Locate and identify every blood parasite.
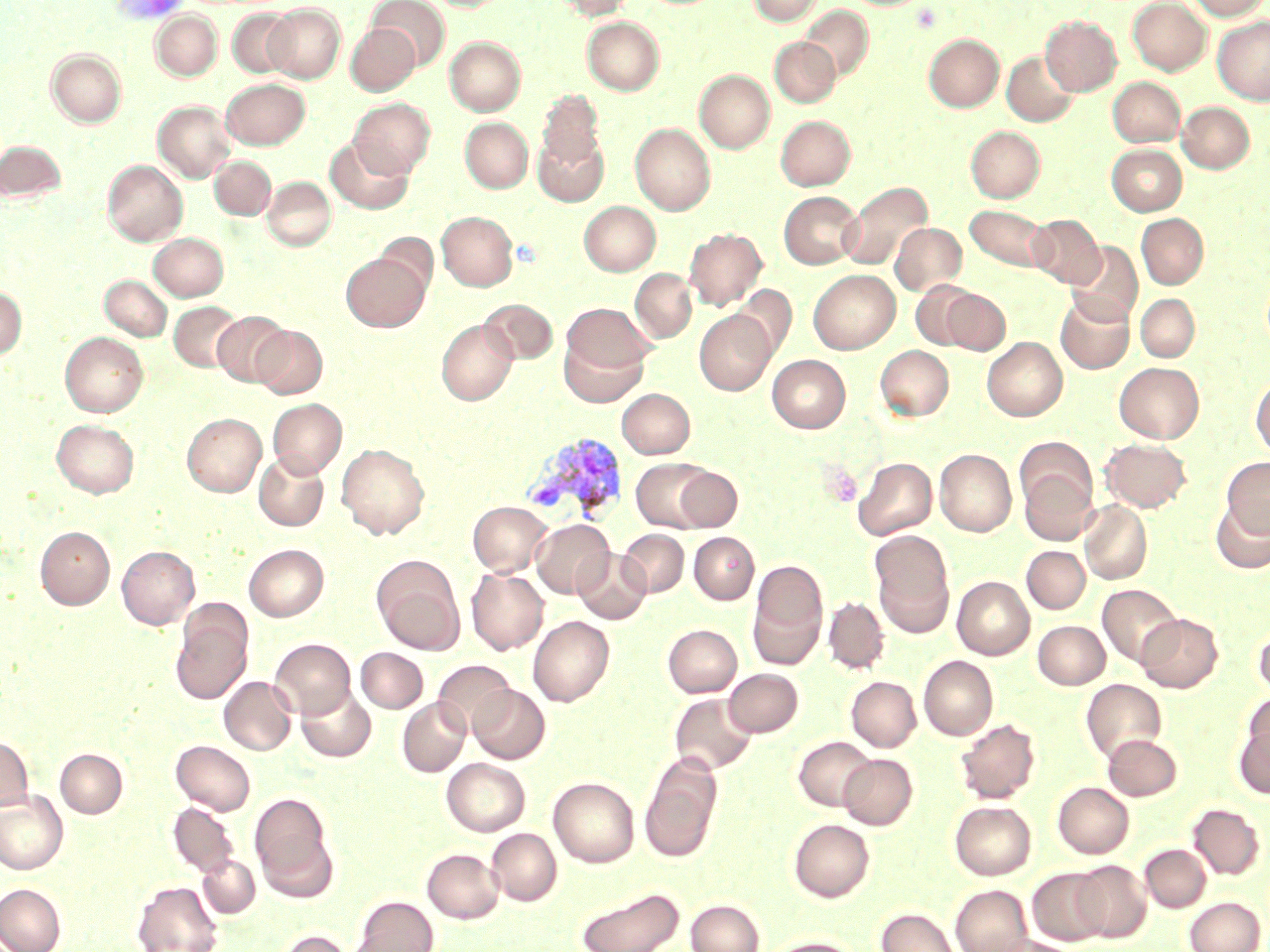

Approximate bounding boxes as [x1, y1, x2, y2] in pixels.
Plasmodium vivax-infected red blood cells: [522, 433, 629, 523].
No Plasmodium falciparum, Plasmodium ovale, Plasmodium malariae, Babesia divergens, or Trypanosoma brucei observed.

Platelet locations: [819, 463, 863, 507]. Uninfected red blood cell locations: [367, 0, 449, 70], [554, 0, 634, 20], [748, 0, 823, 25], [1128, 0, 1211, 75], [1187, 0, 1269, 20], [265, 4, 345, 83], [800, 5, 873, 83], [228, 9, 298, 78], [151, 11, 222, 81], [1041, 16, 1121, 95], [582, 17, 664, 95], [1213, 17, 1270, 104], [346, 24, 420, 95], [924, 34, 1004, 111], [445, 36, 525, 115], [769, 38, 840, 106], [47, 49, 126, 128], [1001, 51, 1078, 126], [695, 70, 774, 153], [1108, 77, 1184, 147], [221, 78, 309, 149], [537, 90, 605, 172], [349, 98, 435, 178], [153, 101, 236, 183], [1177, 102, 1254, 173], [776, 116, 855, 190], [460, 118, 532, 193], [630, 123, 715, 215], [966, 126, 1044, 202], [533, 133, 608, 205], [326, 139, 413, 215], [0, 140, 66, 204], [1107, 144, 1187, 215], [210, 156, 275, 219], [103, 160, 187, 246], [262, 176, 335, 251], [841, 181, 932, 270], [779, 191, 863, 269], [579, 201, 660, 276], [965, 205, 1051, 271], [437, 211, 517, 291], [1136, 213, 1208, 289], [1027, 214, 1105, 287], [890, 223, 967, 295], [685, 228, 767, 310], [148, 232, 228, 301], [1066, 240, 1143, 325], [341, 252, 430, 331], [630, 269, 696, 342], [808, 269, 900, 353], [100, 275, 172, 341], [911, 280, 980, 350], [732, 285, 796, 359], [0, 286, 27, 360], [941, 288, 1010, 354], [1056, 293, 1134, 374], [1135, 294, 1199, 361], [480, 299, 558, 364], [169, 301, 243, 372], [562, 303, 656, 374], [694, 310, 776, 395], [212, 311, 291, 386], [437, 319, 517, 405], [261, 324, 334, 478], [252, 325, 327, 399], [60, 332, 148, 416], [559, 336, 647, 407], [982, 337, 1067, 421], [875, 345, 954, 420], [768, 355, 850, 432], [1114, 362, 1203, 442], [1251, 377, 1270, 457], [617, 388, 695, 458], [268, 399, 347, 478], [182, 413, 266, 496], [52, 420, 139, 497], [1015, 438, 1095, 515], [1100, 438, 1191, 512], [336, 443, 429, 539], [935, 449, 1017, 536], [253, 452, 329, 531], [1221, 457, 1270, 537], [632, 458, 714, 531], [854, 458, 937, 540], [675, 466, 742, 531], [1019, 468, 1098, 545], [1210, 498, 1270, 574], [1079, 500, 1152, 583], [468, 501, 552, 576], [532, 519, 614, 598], [35, 526, 115, 609], [618, 529, 688, 597], [689, 532, 759, 604], [871, 535, 954, 635], [244, 544, 328, 621], [117, 546, 199, 628], [1022, 546, 1090, 613], [573, 548, 651, 624], [373, 558, 464, 654], [748, 559, 828, 667], [466, 568, 549, 654], [952, 576, 1035, 659], [1098, 584, 1182, 666], [824, 597, 888, 673], [171, 607, 253, 704], [1136, 614, 1223, 692], [528, 616, 614, 706], [1033, 621, 1110, 689], [1254, 621, 1270, 698], [663, 624, 741, 697], [270, 638, 356, 719], [356, 648, 428, 712], [919, 655, 997, 740], [433, 660, 515, 736], [724, 669, 803, 736], [220, 676, 296, 755], [846, 676, 921, 751], [1081, 679, 1166, 762], [297, 685, 376, 762], [469, 685, 550, 763], [669, 693, 757, 775], [1243, 695, 1270, 763], [398, 698, 471, 777], [955, 719, 1039, 803], [1234, 724, 1270, 798], [1103, 734, 1181, 800], [0, 735, 33, 812], [794, 736, 876, 810], [171, 740, 255, 815], [55, 748, 127, 818], [639, 753, 723, 863], [839, 754, 916, 829], [441, 758, 530, 836], [549, 777, 639, 867], [1053, 782, 1133, 858], [0, 790, 68, 874], [250, 793, 336, 895], [950, 801, 1035, 879], [169, 802, 239, 877], [1188, 803, 1265, 879], [789, 819, 874, 902], [487, 828, 562, 905], [1141, 844, 1211, 912], [423, 849, 504, 922], [198, 855, 259, 917], [1071, 860, 1151, 942], [1027, 867, 1110, 945], [133, 881, 223, 952], [0, 883, 65, 952], [950, 885, 1033, 952], [576, 886, 685, 952], [353, 896, 438, 952], [1185, 897, 1264, 952], [686, 899, 763, 952], [877, 908, 960, 952], [277, 930, 353, 952], [990, 936, 1077, 952], [764, 937, 859, 952]. Slide-level diagnosis: Plasmodium vivax. May-Grünwald-Giemsa stain. One field of a larger specimen. Image is 1270×952 pixels. 1000x magnification. Optical microscopy. Thin blood film.